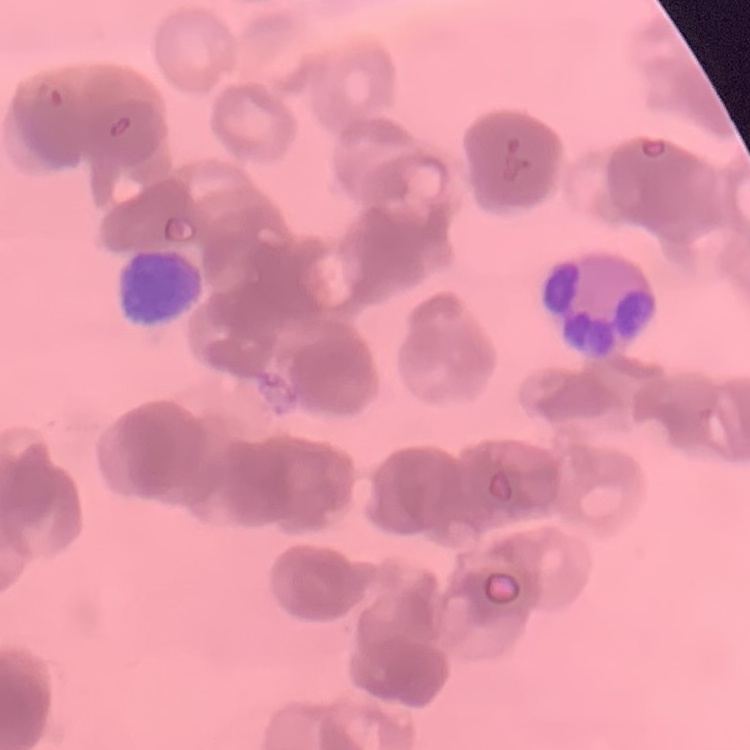
{
  "erythrocyte_morphology": "rouleaux formation",
  "stain": "Field's or Giemsa",
  "image_type": "square crop of a larger photomicrograph",
  "preparation": "thin peripheral smear"
}